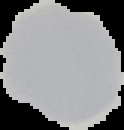
Summary:
  - Image type: segmented cell region with the area outside set to black
  - Preparation: thin blood smear
  - Malaria status: uninfected
  - Image size: 124×130 pixels